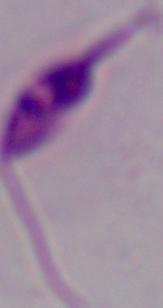
A Leishmania parasite is seen. 1000x magnification. Micrograph.